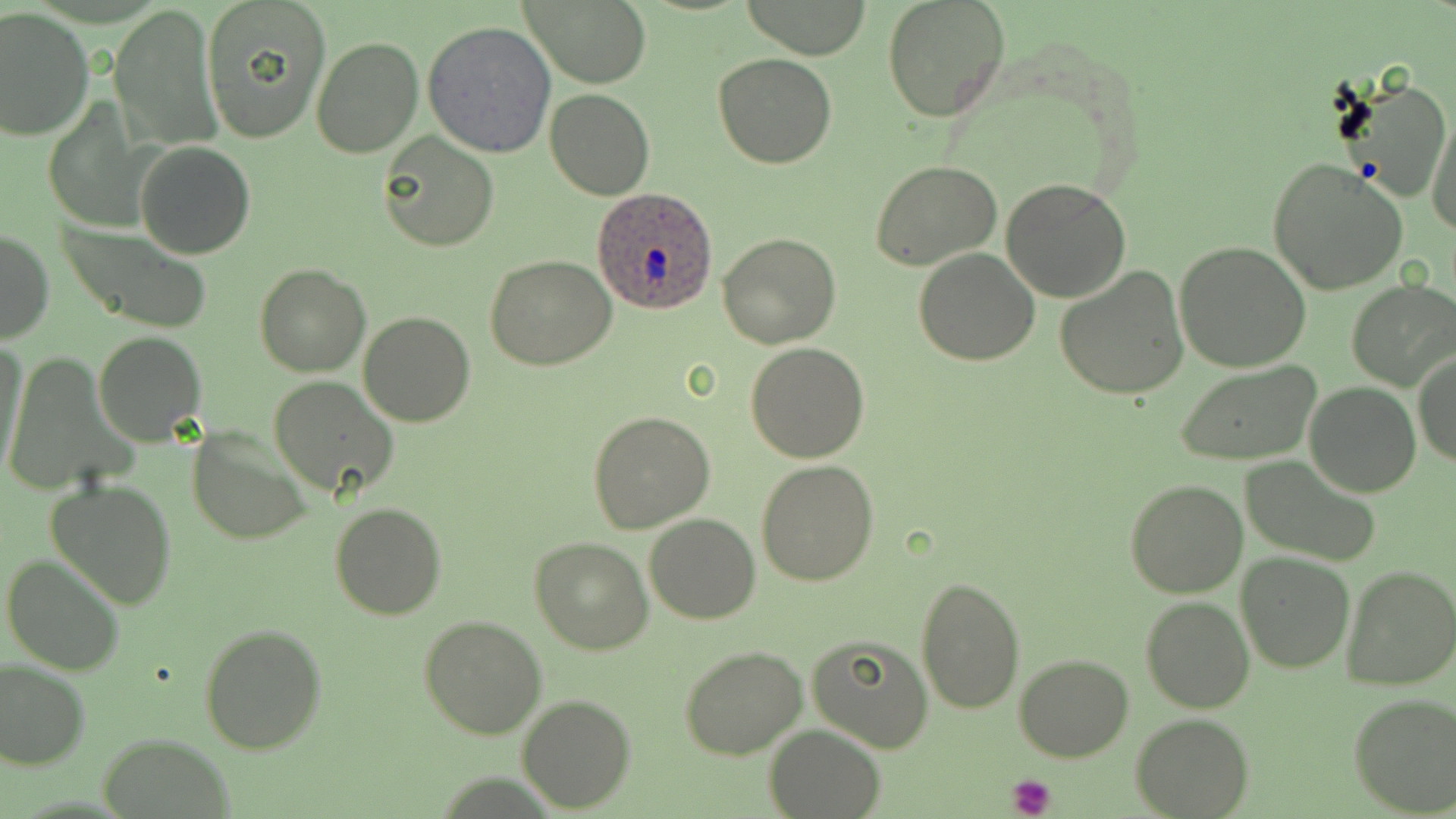 Approximate bounding boxes as [x1, y1, x2, y2] in pixels. Plasmodium ovale-infected red blood cell locations: [593, 187, 721, 317]. Uninfected red blood cell locations: [201, 0, 331, 144], [522, 0, 652, 89], [738, 0, 875, 59], [882, 0, 1011, 121], [110, 5, 222, 154], [0, 9, 95, 142], [423, 20, 556, 158], [310, 35, 424, 157], [714, 52, 836, 168], [1335, 76, 1453, 206], [545, 88, 655, 200], [43, 105, 149, 230], [1427, 107, 1456, 239], [378, 131, 499, 251], [135, 141, 255, 259], [1265, 158, 1411, 297], [871, 160, 1003, 271], [1001, 178, 1132, 301], [57, 223, 212, 332], [1, 230, 53, 344], [718, 233, 839, 348], [1174, 241, 1311, 372], [913, 249, 1041, 366], [485, 256, 618, 371], [254, 264, 370, 378], [1053, 266, 1190, 399], [1347, 281, 1456, 391], [357, 312, 477, 427], [93, 331, 206, 445], [0, 339, 29, 485], [746, 343, 869, 462], [1412, 351, 1456, 470], [1, 355, 136, 497], [1174, 362, 1325, 468], [268, 375, 398, 497], [1304, 382, 1420, 497], [587, 411, 715, 533], [188, 427, 310, 545], [1243, 456, 1382, 566], [756, 459, 881, 587], [47, 478, 177, 610], [1124, 479, 1248, 598], [330, 502, 447, 621], [644, 512, 761, 624], [529, 537, 654, 656], [2, 553, 126, 677], [1236, 553, 1354, 673], [1341, 565, 1456, 690], [914, 576, 1026, 716], [1140, 595, 1254, 713], [419, 614, 547, 739], [199, 624, 328, 754], [805, 635, 932, 752], [679, 645, 807, 759], [1015, 653, 1135, 762], [0, 660, 89, 771], [517, 693, 635, 811], [1347, 693, 1456, 818], [1130, 712, 1254, 818], [762, 724, 885, 819], [99, 734, 235, 819]. Platelet locations: [1008, 774, 1057, 819]. Slide-level diagnosis: Plasmodium ovale. 1000x magnification. Image is 1456×819 pixels. Light microscopy. One field of a larger specimen. May-Grünwald-Giemsa-stained preparation. Thin blood smear.